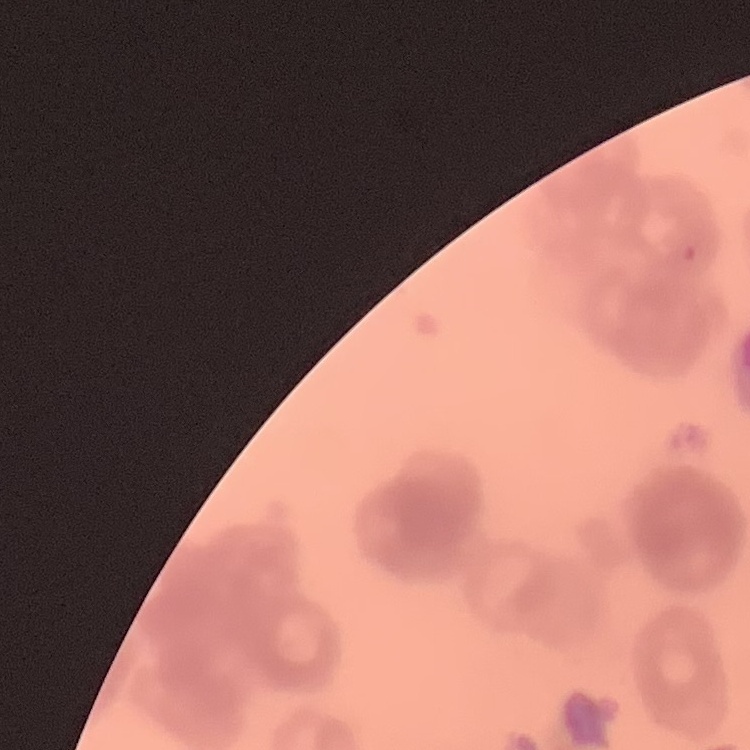
The erythrocytes exhibit rouleaux formation. Square crop of a larger photomicrograph. Field's or Giemsa stain. Thin blood film.